Comment on the morphology of the red blood cells.
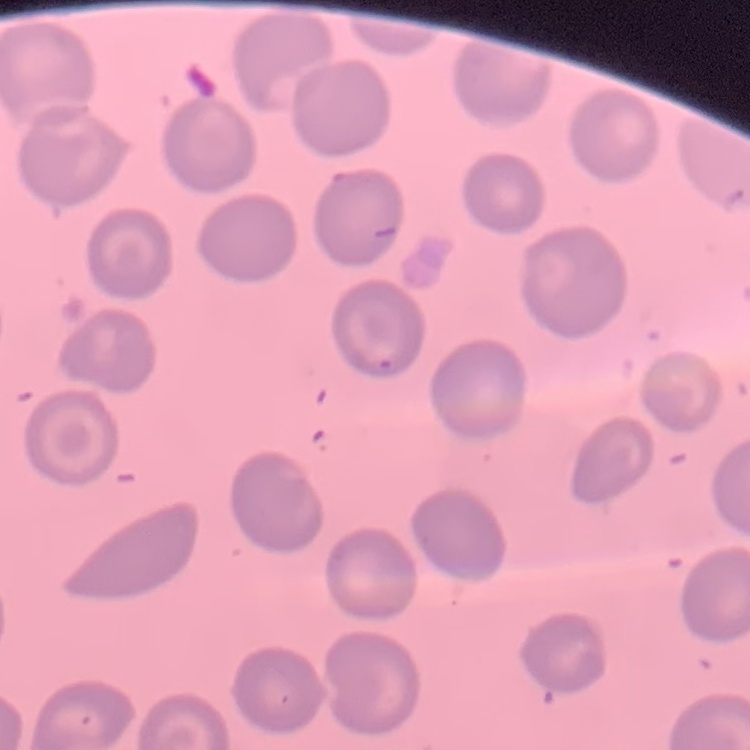
No rouleaux formation.

preparation: thin blood film
image_type: square crop of a larger photomicrograph
stain: Field's or Giemsa